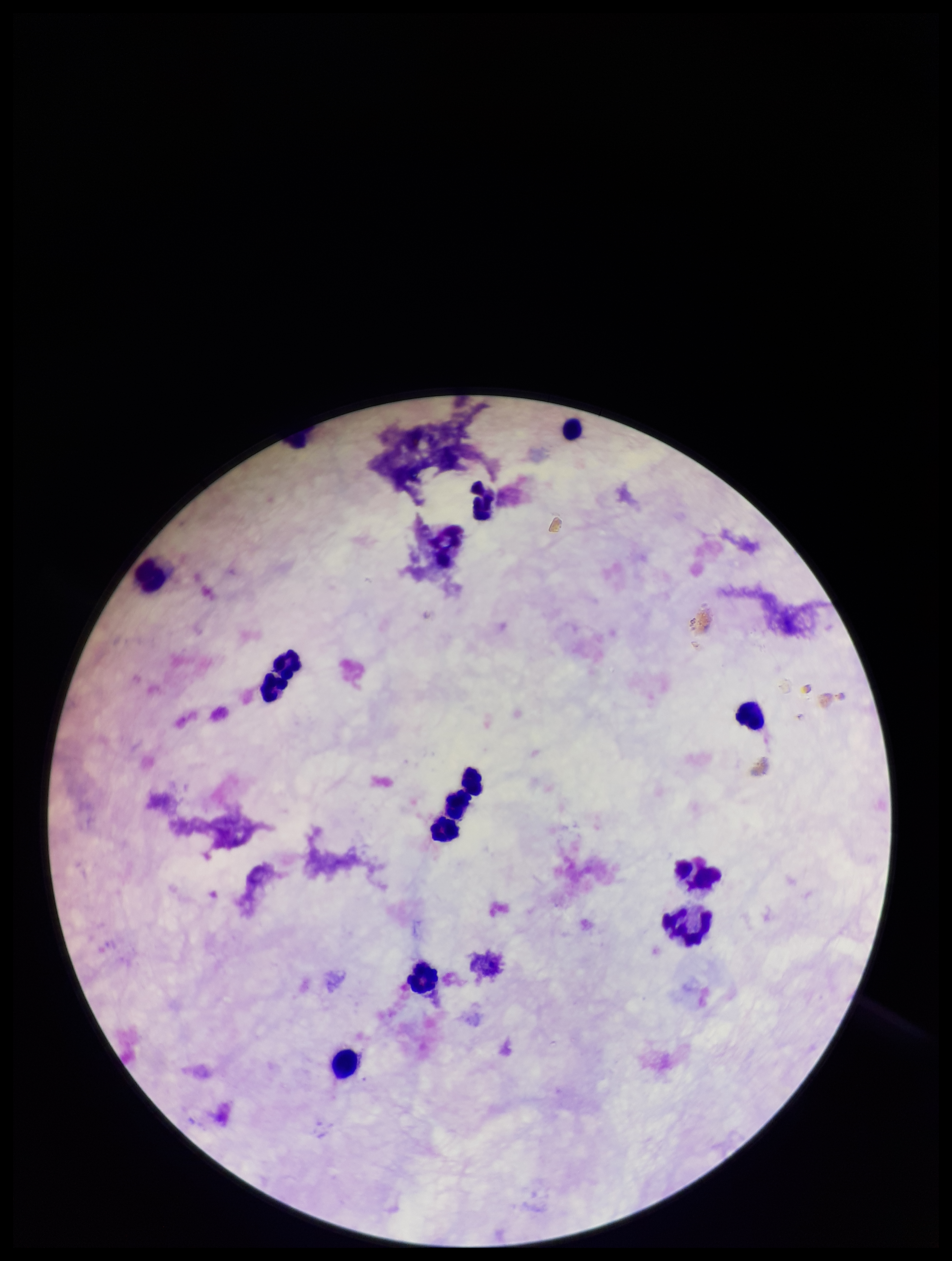

{
  "stain": "Giemsa",
  "image_size": "952×1261 pixels",
  "parasite_count": 0,
  "plasmodium_parasites": "none identified",
  "field_of_view": "one from this slide",
  "patient_malaria_status": "negative",
  "capture": "smartphone photograph through the microscope eyepiece",
  "preparation": "thick smear",
  "leukocyte_count": 12
}